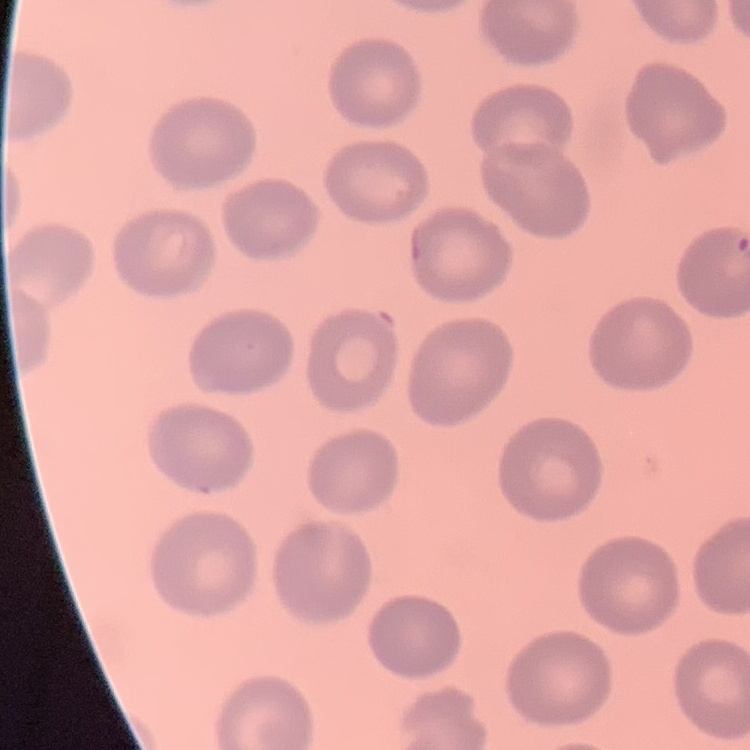

The erythrocytes show no rouleaux formation. Square crop of a larger photomicrograph. Stained with either Field's or Giemsa. Thin peripheral smear.